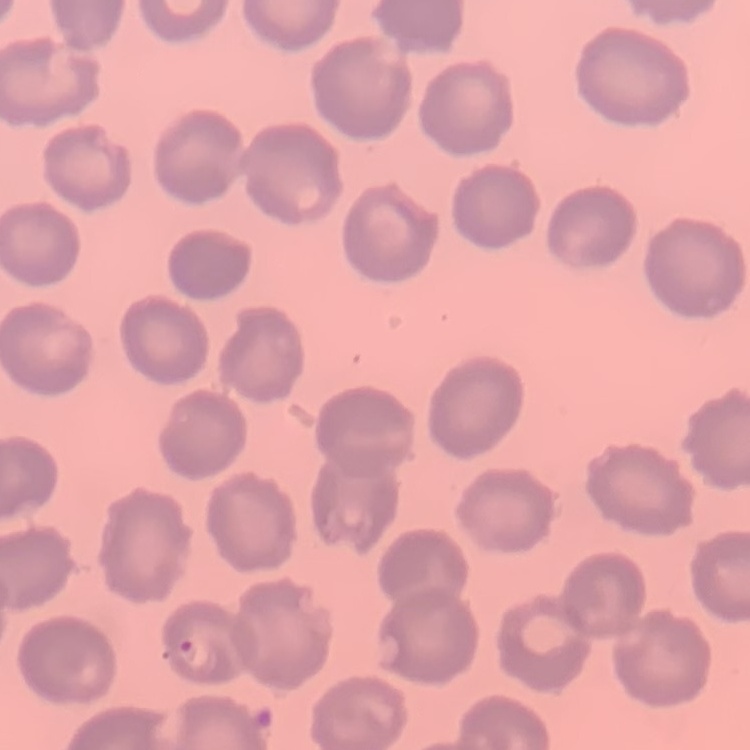
{
  "erythrocyte_morphology": "no rouleaux formation",
  "preparation": "thin blood film",
  "stain": "Field's or Giemsa",
  "image_type": "one tile cut from a larger photomicrograph"
}